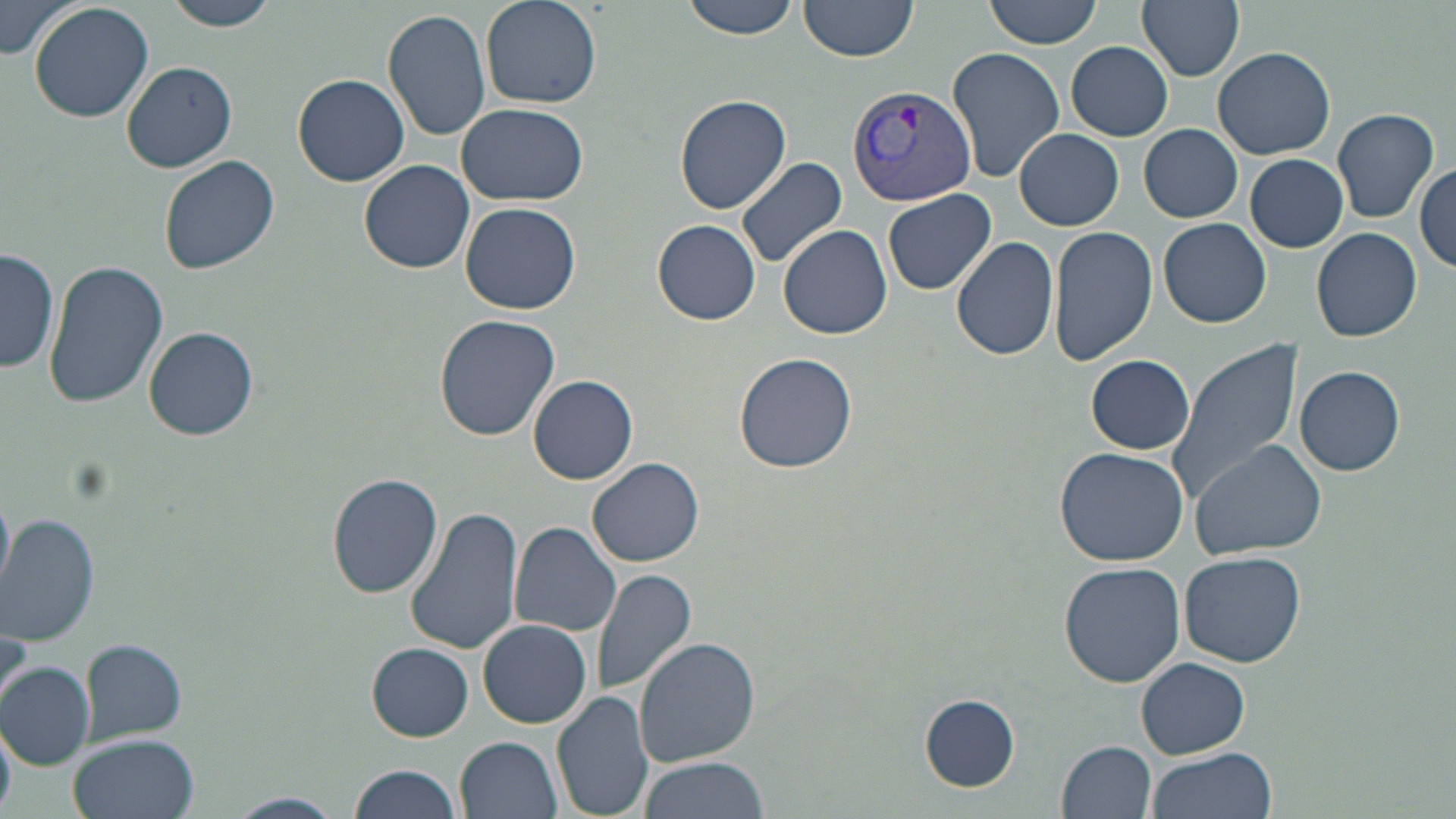 Approximate bounding boxes as (x1,y1)-(x2,y2) corner pairs in pixels. Plasmodium vivax-infected red blood cell locations: (846,83)-(975,208). Uninfected red blood cell locations: (1,0)-(76,60), (28,0)-(154,122), (161,0)-(286,31), (481,0)-(602,110), (680,0)-(803,40), (798,0)-(919,61), (985,0)-(1102,49), (1137,0)-(1244,80), (381,8)-(491,143), (1066,42)-(1173,140), (948,47)-(1065,182), (1214,47)-(1335,159), (119,62)-(238,172), (294,73)-(409,186), (673,95)-(791,215), (456,103)-(587,206), (1331,107)-(1440,224), (1139,124)-(1242,222), (1014,129)-(1123,229), (1245,153)-(1348,252), (159,156)-(280,276), (737,156)-(847,271), (359,160)-(476,274), (1416,160)-(1455,272), (883,189)-(996,295), (459,203)-(581,314), (1158,217)-(1272,328), (652,218)-(761,325), (778,224)-(893,339), (1049,225)-(1158,365), (1312,227)-(1422,341), (951,236)-(1060,360), (1,249)-(59,376), (43,260)-(168,408), (435,315)-(560,441), (145,327)-(258,440), (1166,340)-(1303,504), (733,350)-(858,473), (1085,354)-(1195,454), (1294,364)-(1405,476), (529,375)-(638,485), (1189,439)-(1327,559), (1055,447)-(1189,566), (588,457)-(704,567), (327,473)-(443,598), (0,490)-(13,595), (405,505)-(525,657), (0,513)-(99,646), (510,521)-(624,637), (1179,550)-(1307,667), (1058,562)-(1185,685), (591,567)-(696,696), (479,619)-(592,728), (0,622)-(30,712), (634,638)-(760,768), (80,640)-(186,742), (367,643)-(474,741), (1137,657)-(1251,758), (0,663)-(93,770), (552,689)-(654,819), (918,693)-(1020,793), (0,722)-(16,815), (70,734)-(198,819), (457,736)-(563,819), (1057,740)-(1157,818), (1144,749)-(1276,819), (637,755)-(772,819), (348,763)-(464,819), (224,792)-(346,819). Slide-level diagnosis: Plasmodium vivax. 1000x magnification. Thin blood smear. One field of a larger specimen. Image is 1456×819 pixels. May-Grünwald-Giemsa-stained preparation. Light microscopy.